Assess the morphology of the erythrocytes.
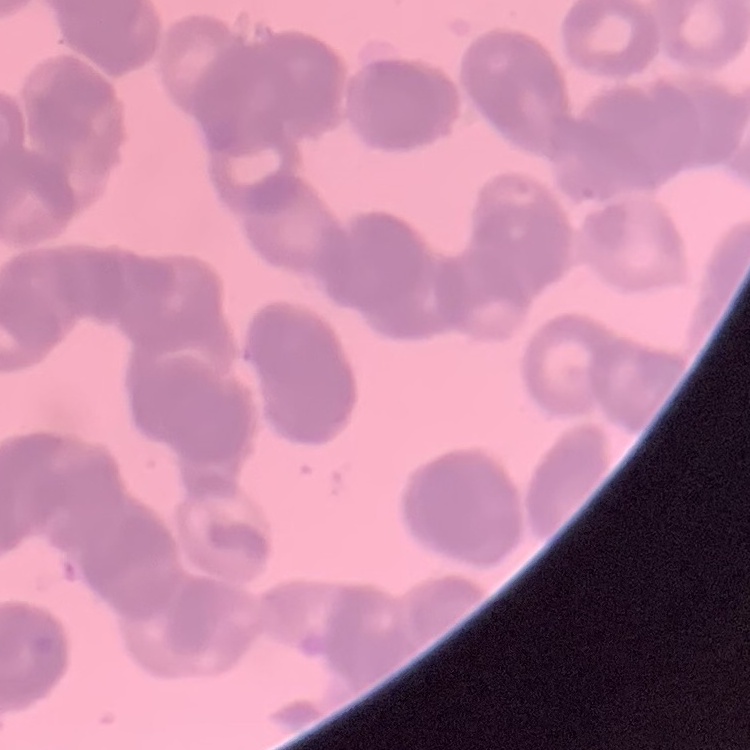

Rouleaux formation.

image type = square crop of a larger photomicrograph
stain = Field's or Giemsa
preparation = thin blood smear